Classify this cell by malaria status.
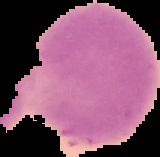

It is uninfected.

Cell region segmented out of the field of view; the surrounding area is masked to black. Image is 160×157 pixels. From a thin blood smear.